Classify this cell by malaria status.
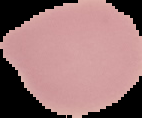
It is uninfected.

Image is 142×118 pixels. Cell region segmented out of the field of view; the surrounding area is masked to black. From a thin blood smear.